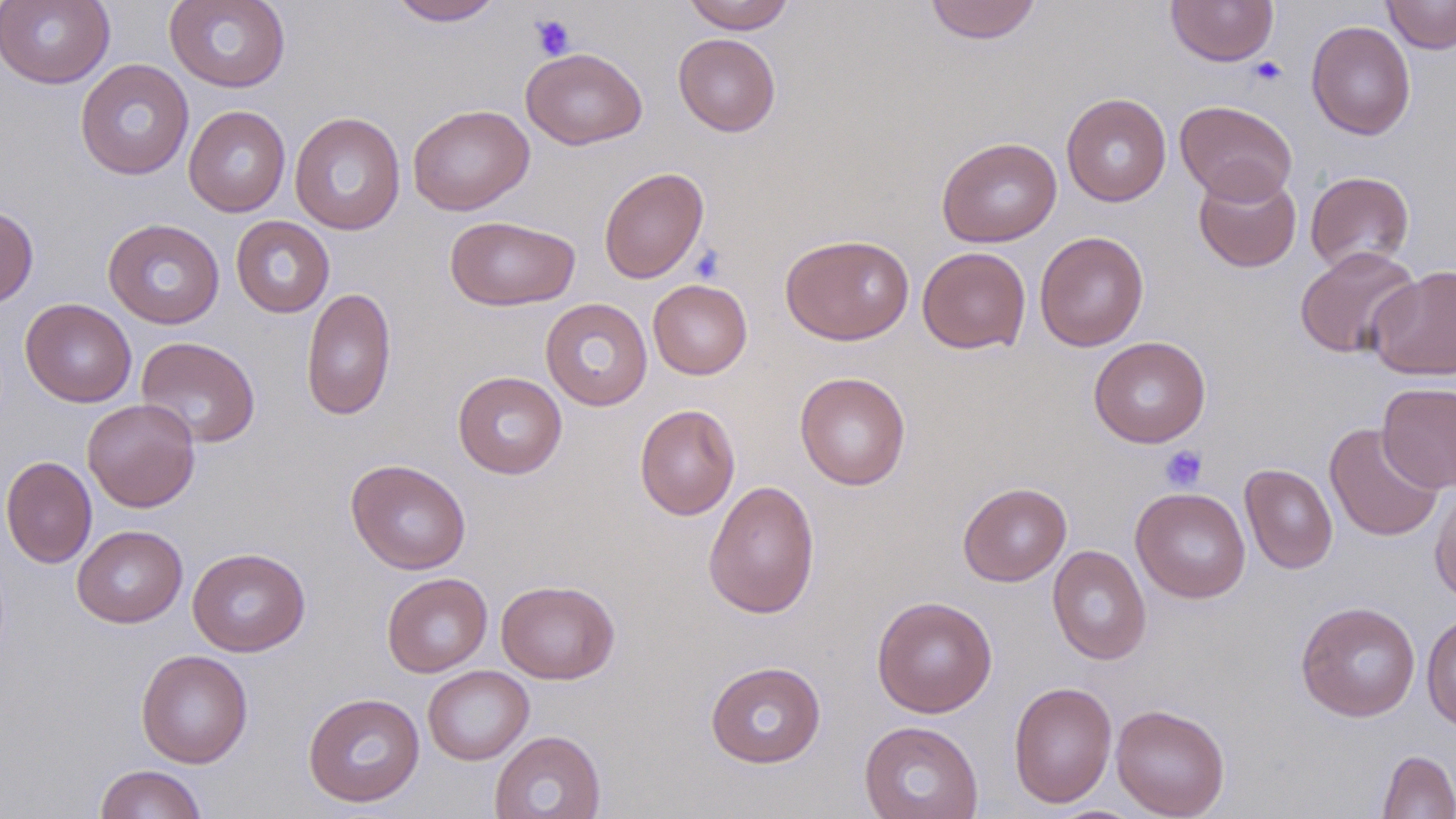

slide-level diagnosis = no evidence of blood parasites
field of view = single
uninfected red blood cell locations = approximate bounding boxes as [x1, y1, x2, y2] in pixels: [0, 0, 115, 89], [164, 0, 291, 93], [387, 0, 504, 26], [681, 0, 796, 32], [924, 0, 1042, 44], [1165, 0, 1279, 66], [1382, 0, 1456, 53], [1306, 21, 1416, 140], [673, 33, 781, 136], [521, 47, 647, 150], [75, 59, 194, 180], [1061, 92, 1172, 207], [1175, 100, 1297, 204], [408, 104, 534, 215], [183, 105, 290, 217], [289, 111, 405, 235], [937, 136, 1062, 247], [598, 167, 709, 284], [1193, 170, 1301, 272], [1305, 171, 1415, 273], [0, 206, 39, 308], [444, 215, 579, 311], [231, 216, 334, 317], [103, 218, 225, 329], [1034, 231, 1149, 351], [780, 233, 915, 345], [1294, 246, 1422, 359], [917, 247, 1030, 354], [1368, 265, 1456, 381], [648, 279, 752, 379], [301, 287, 397, 421], [20, 298, 136, 407], [540, 298, 653, 411], [136, 336, 261, 448], [1088, 336, 1211, 448], [452, 371, 567, 479], [794, 372, 910, 490], [1376, 382, 1456, 493], [82, 398, 200, 512], [635, 404, 741, 520], [1324, 422, 1444, 542], [1, 456, 97, 568], [346, 459, 471, 574], [1240, 463, 1338, 574], [702, 479, 820, 619], [1430, 481, 1456, 605], [958, 482, 1072, 586], [1131, 487, 1251, 604], [72, 524, 188, 628], [1047, 545, 1151, 665], [187, 547, 310, 657], [382, 572, 492, 677], [496, 579, 620, 684], [872, 596, 998, 717], [1296, 601, 1421, 722], [1421, 611, 1456, 731], [136, 649, 253, 768], [705, 660, 826, 768], [422, 665, 534, 765], [1008, 682, 1118, 808], [303, 692, 425, 807], [1111, 703, 1230, 819], [858, 720, 983, 819], [489, 729, 606, 819], [1377, 750, 1456, 819], [93, 764, 208, 819]
image size = 1456×819 pixels
magnification = 1000x
preparation = thin blood film
platelet locations = approximate bounding boxes as [x1, y1, x2, y2] in pixels: [531, 14, 575, 59], [1247, 56, 1288, 87], [690, 244, 727, 285], [1159, 444, 1207, 492]
modality = light microscopy
stain = May-Grünwald-Giemsa